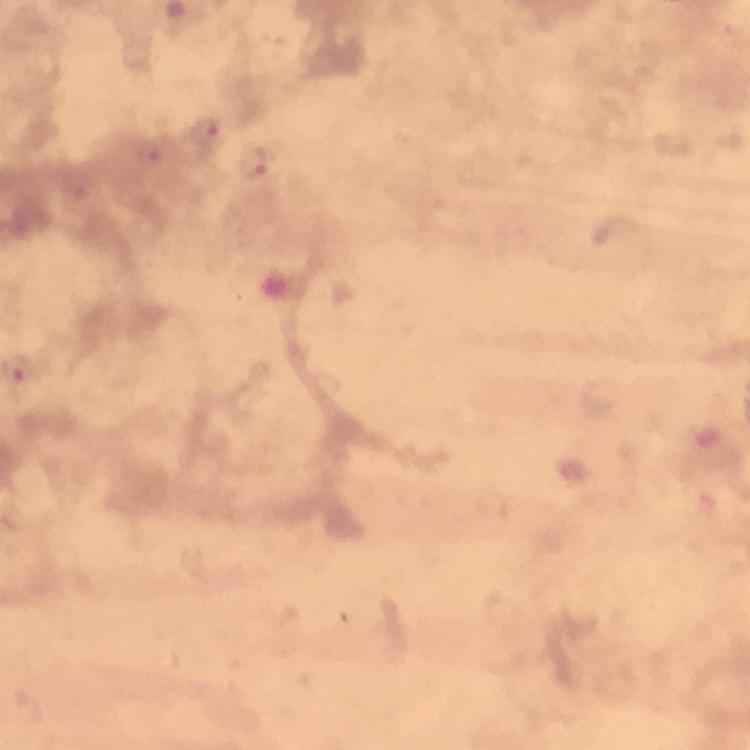

Approximate centers as [x, y] in pixels.
Summary:
  - Plasmodium parasite locations: [205, 132], [253, 164]
  - Image size: 750×750 pixels
  - Preparation: thick smear
  - Immersion oil: applied
  - Capture: smartphone mounted on the microscope
  - Cropped from: one field of view
  - Context: from a malaria diagnostic workup
  - Magnification: 100x
  - Stain: Giemsa